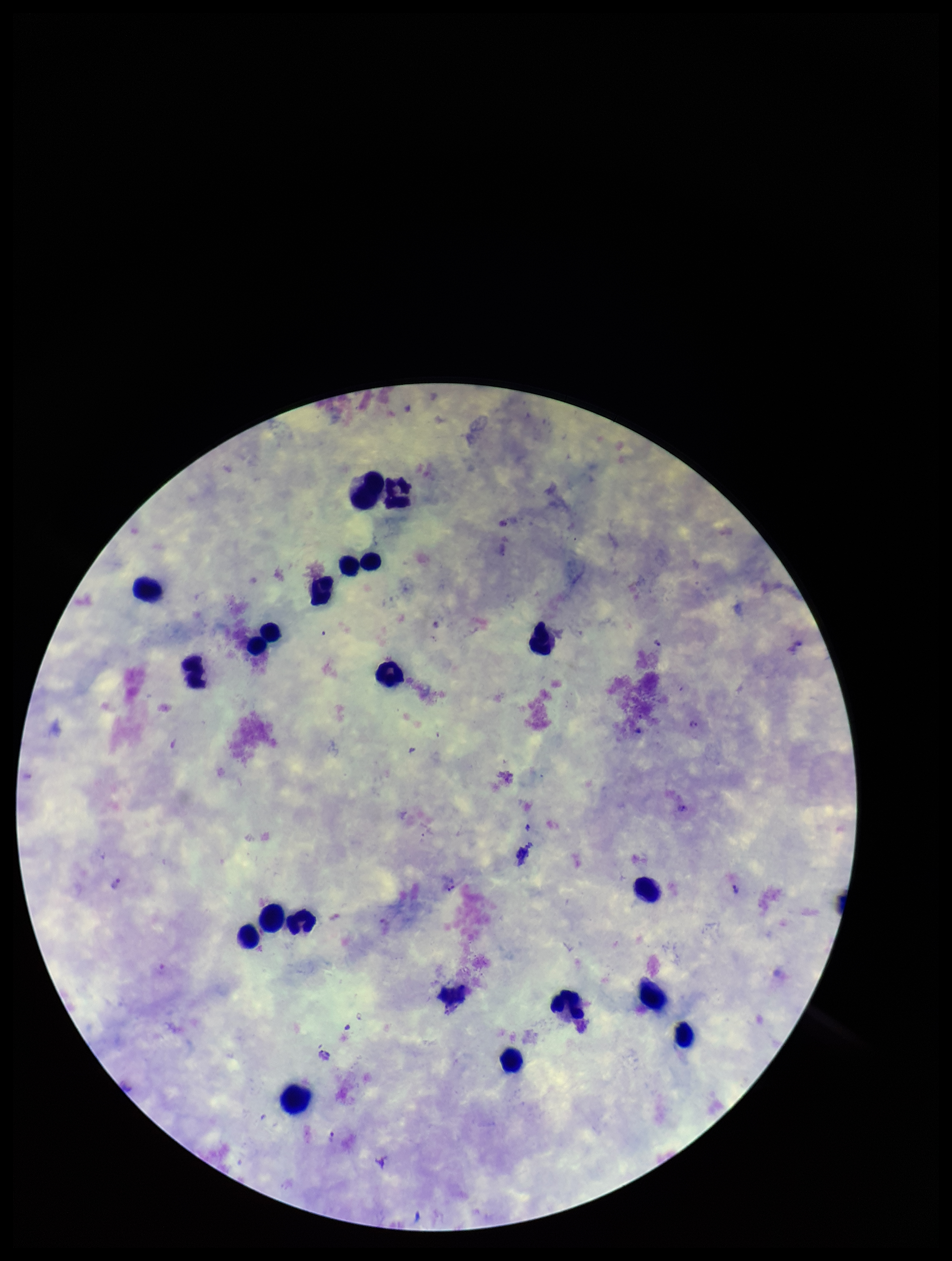

Image is 952×1261 pixels. Leukocyte count: 19. Species reported for this patient: Plasmodium vivax. Stained with Giemsa. Plasmodium parasites: seen. Photographed through the microscope eyepiece with a smartphone camera. Preparation: thick blood smear. Parasite count: 6. Patient malaria status: infected. One field from this slide.